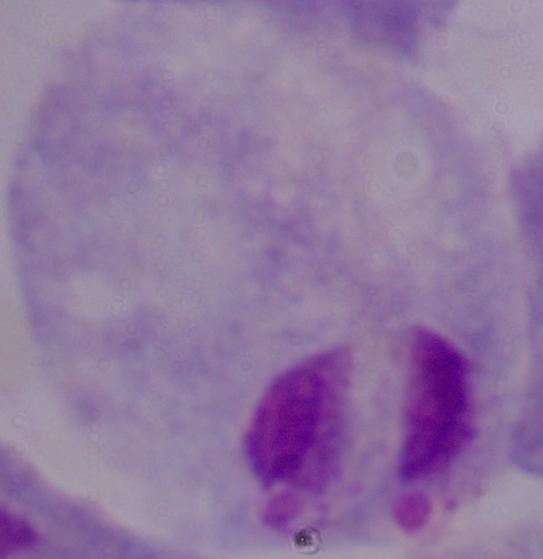

Micrograph. A trichomonad is seen. Captured at 1000x magnification.